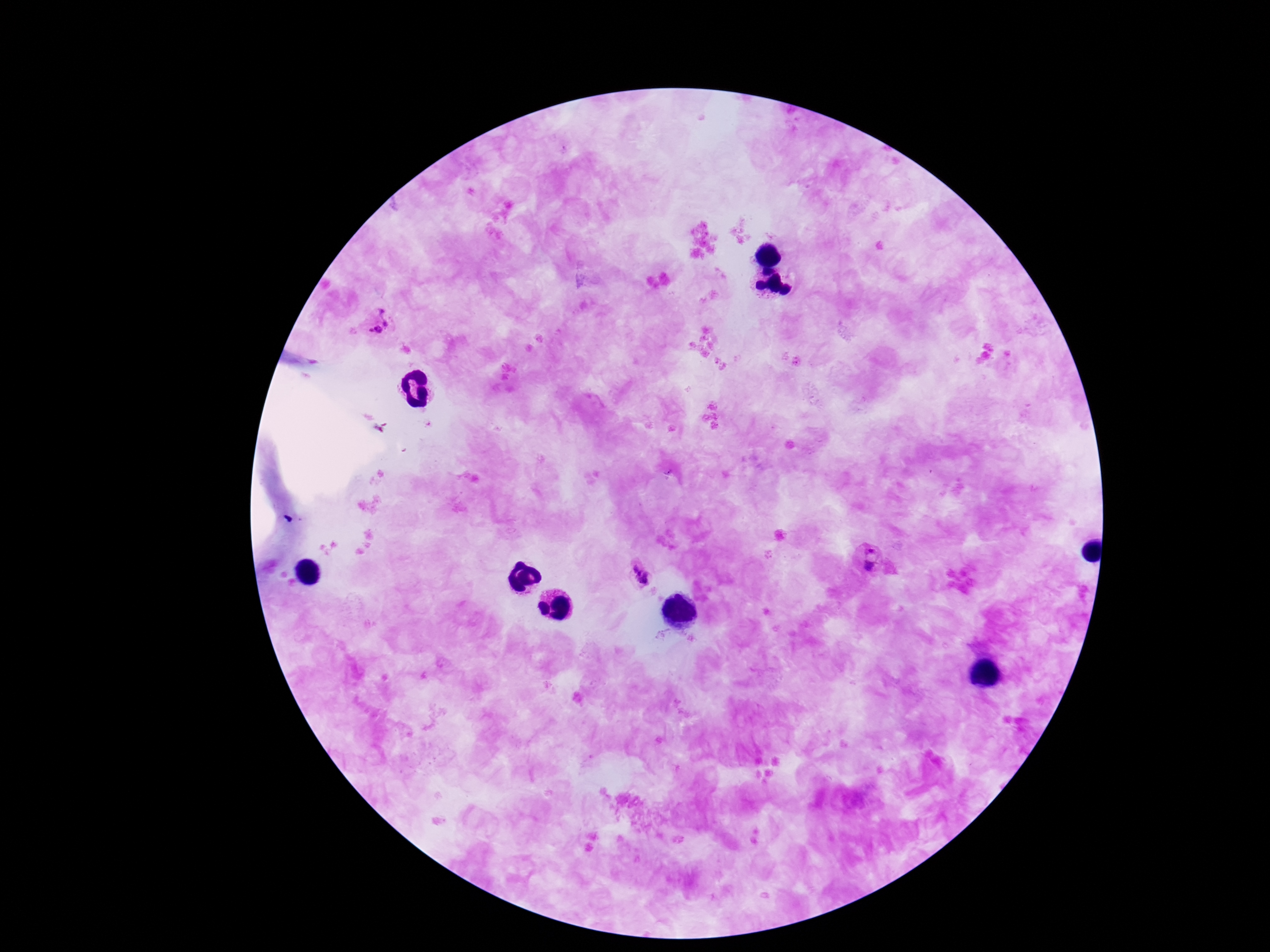 Approximate object centers, in pixels from the top-left corner. Plasmodium parasite locations: (x=379, y=325), (x=869, y=561), (x=639, y=576). Patient malaria status: infected. One field from this slide. Photographed through the microscope eyepiece with a smartphone camera. 100x magnification. Thick blood smear. Giemsa stain. Image is 1270×952 pixels.